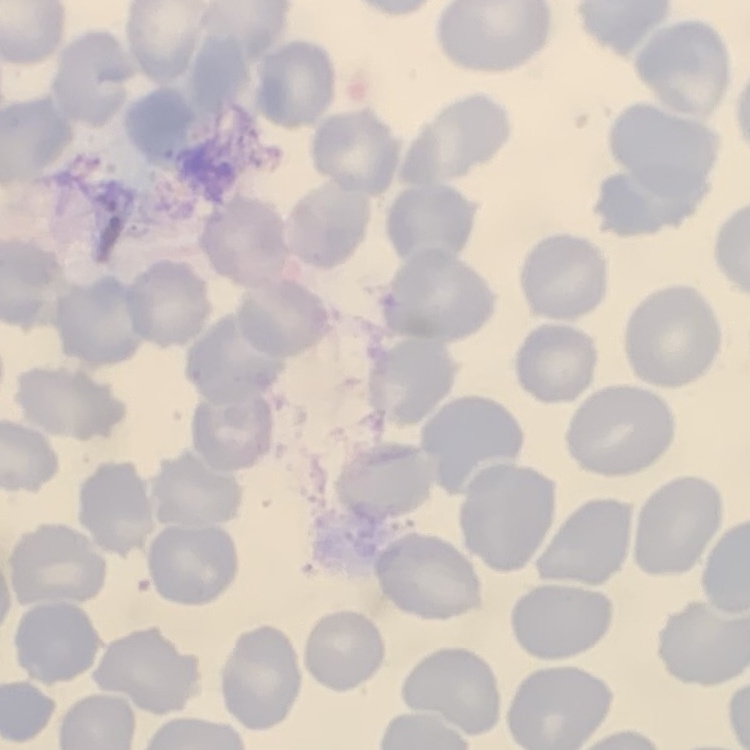

erythrocyte_morphology: no rouleaux formation
image_type: square crop of a larger photomicrograph
stain: Field's or Giemsa
preparation: thin blood smear